Name the parasite shown.
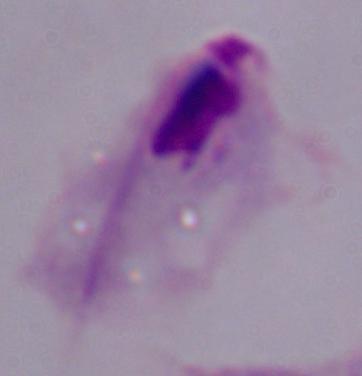

This is a trichomonad.

Micrograph. 1000x magnification.